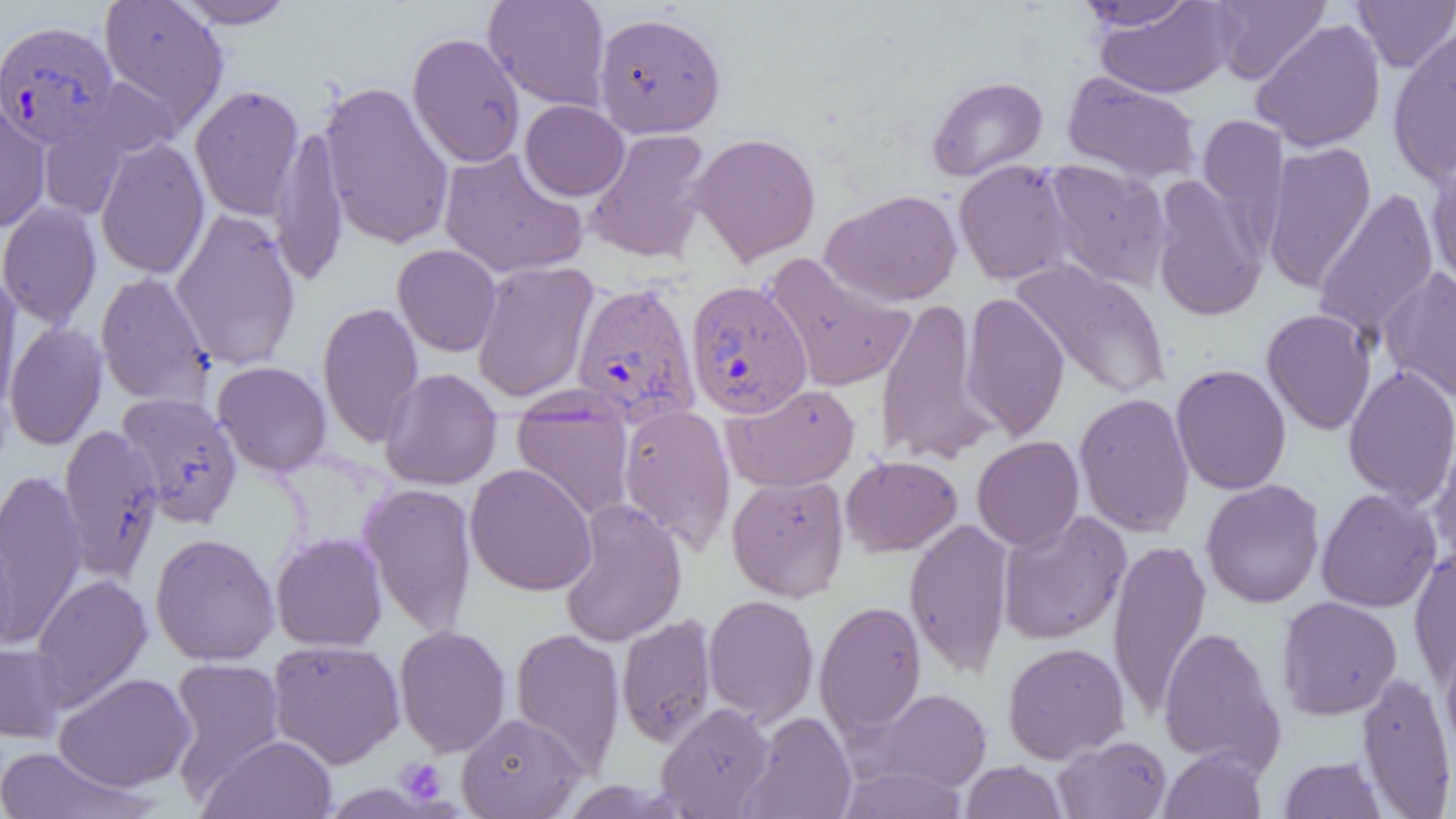

slide-level diagnosis = Plasmodium vivax
field of view = one of a larger specimen
Plasmodium vivax-infected red blood cell locations = approximate bounding boxes as named x1/y1/x2/y2 corners in pixels: (x1=0, y1=19, x2=120, y2=150), (x1=685, y1=280, x2=813, y2=419), (x1=570, y1=281, x2=701, y2=427)
magnification = 1000x
preparation = thin blood smear
image size = 1456×819 pixels
uninfected red blood cell locations = approximate bounding boxes as named x1/y1/x2/y2 corners in pixels: (x1=98, y1=0, x2=229, y2=132), (x1=172, y1=0, x2=297, y2=29), (x1=483, y1=0, x2=611, y2=111), (x1=1073, y1=0, x2=1202, y2=31), (x1=1209, y1=0, x2=1331, y2=84), (x1=1093, y1=1, x2=1238, y2=98), (x1=1353, y1=1, x2=1456, y2=72), (x1=593, y1=11, x2=726, y2=138), (x1=1250, y1=18, x2=1386, y2=152), (x1=1386, y1=25, x2=1456, y2=186), (x1=407, y1=32, x2=525, y2=168), (x1=1062, y1=71, x2=1202, y2=183), (x1=926, y1=76, x2=1048, y2=181), (x1=318, y1=79, x2=455, y2=251), (x1=189, y1=84, x2=305, y2=221), (x1=0, y1=99, x2=51, y2=233), (x1=520, y1=100, x2=630, y2=201), (x1=1198, y1=113, x2=1289, y2=237), (x1=36, y1=116, x2=131, y2=220), (x1=270, y1=125, x2=349, y2=286), (x1=584, y1=128, x2=713, y2=264), (x1=689, y1=132, x2=822, y2=266), (x1=95, y1=136, x2=210, y2=279), (x1=1262, y1=141, x2=1376, y2=293), (x1=437, y1=147, x2=588, y2=279), (x1=1426, y1=150, x2=1456, y2=296), (x1=953, y1=159, x2=1075, y2=286), (x1=1042, y1=159, x2=1173, y2=290), (x1=1150, y1=174, x2=1268, y2=322), (x1=1312, y1=187, x2=1441, y2=346), (x1=821, y1=188, x2=963, y2=306), (x1=0, y1=202, x2=102, y2=329), (x1=170, y1=208, x2=302, y2=370), (x1=392, y1=244, x2=502, y2=356), (x1=763, y1=253, x2=917, y2=393), (x1=471, y1=260, x2=599, y2=403), (x1=1010, y1=260, x2=1171, y2=400), (x1=1379, y1=267, x2=1456, y2=401), (x1=95, y1=272, x2=214, y2=406), (x1=0, y1=273, x2=23, y2=417), (x1=960, y1=292, x2=1070, y2=441), (x1=874, y1=296, x2=996, y2=466), (x1=317, y1=301, x2=423, y2=448), (x1=1261, y1=308, x2=1376, y2=435), (x1=4, y1=321, x2=108, y2=450), (x1=212, y1=361, x2=332, y2=476), (x1=1170, y1=363, x2=1291, y2=495), (x1=1342, y1=366, x2=1456, y2=507), (x1=379, y1=368, x2=502, y2=491), (x1=721, y1=382, x2=860, y2=492), (x1=116, y1=392, x2=243, y2=527), (x1=1073, y1=392, x2=1195, y2=537), (x1=511, y1=395, x2=635, y2=521), (x1=616, y1=403, x2=737, y2=554), (x1=58, y1=423, x2=163, y2=579), (x1=1429, y1=428, x2=1456, y2=567), (x1=972, y1=436, x2=1085, y2=551), (x1=840, y1=454, x2=963, y2=557), (x1=464, y1=463, x2=597, y2=596), (x1=0, y1=470, x2=87, y2=644), (x1=726, y1=473, x2=851, y2=601), (x1=1200, y1=479, x2=1325, y2=608), (x1=358, y1=482, x2=478, y2=637), (x1=1316, y1=488, x2=1442, y2=613), (x1=558, y1=498, x2=687, y2=648), (x1=997, y1=510, x2=1132, y2=645), (x1=904, y1=517, x2=1014, y2=677), (x1=0, y1=532, x2=18, y2=657), (x1=150, y1=532, x2=280, y2=665), (x1=270, y1=533, x2=388, y2=652), (x1=1107, y1=540, x2=1212, y2=717), (x1=1409, y1=544, x2=1456, y2=686), (x1=30, y1=573, x2=153, y2=709), (x1=703, y1=594, x2=819, y2=725), (x1=1276, y1=595, x2=1403, y2=720), (x1=815, y1=599, x2=927, y2=738), (x1=616, y1=613, x2=717, y2=747), (x1=393, y1=624, x2=511, y2=757), (x1=1158, y1=625, x2=1285, y2=773), (x1=509, y1=627, x2=625, y2=775), (x1=266, y1=639, x2=405, y2=768), (x1=1440, y1=640, x2=1456, y2=763), (x1=1002, y1=641, x2=1130, y2=763), (x1=0, y1=642, x2=68, y2=743), (x1=166, y1=657, x2=285, y2=799), (x1=1356, y1=670, x2=1456, y2=818), (x1=53, y1=672, x2=196, y2=792), (x1=864, y1=687, x2=992, y2=792), (x1=656, y1=702, x2=775, y2=818), (x1=740, y1=711, x2=857, y2=819), (x1=457, y1=712, x2=585, y2=818), (x1=198, y1=734, x2=338, y2=818), (x1=1053, y1=735, x2=1172, y2=818), (x1=0, y1=746, x2=156, y2=818), (x1=1159, y1=747, x2=1267, y2=819), (x1=1278, y1=755, x2=1388, y2=818), (x1=961, y1=760, x2=1067, y2=819), (x1=837, y1=765, x2=968, y2=818)
modality = light microscopy
platelet locations = approximate bounding boxes as named x1/y1/x2/y2 corners in pixels: (x1=395, y1=757, x2=448, y2=805)